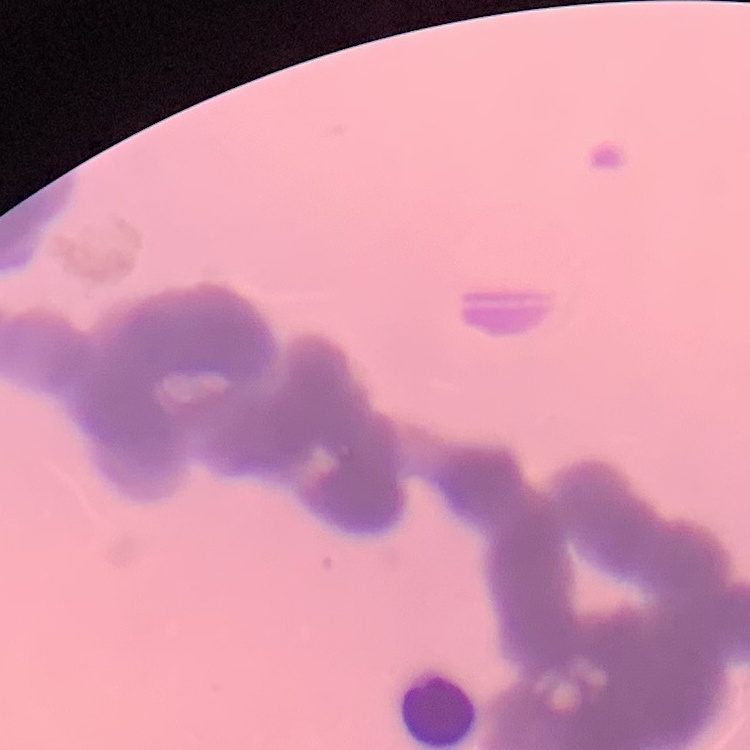 The erythrocytes exhibit rouleaux formation. Square crop of a larger photomicrograph. Thin peripheral smear. Field's or Giemsa stain.